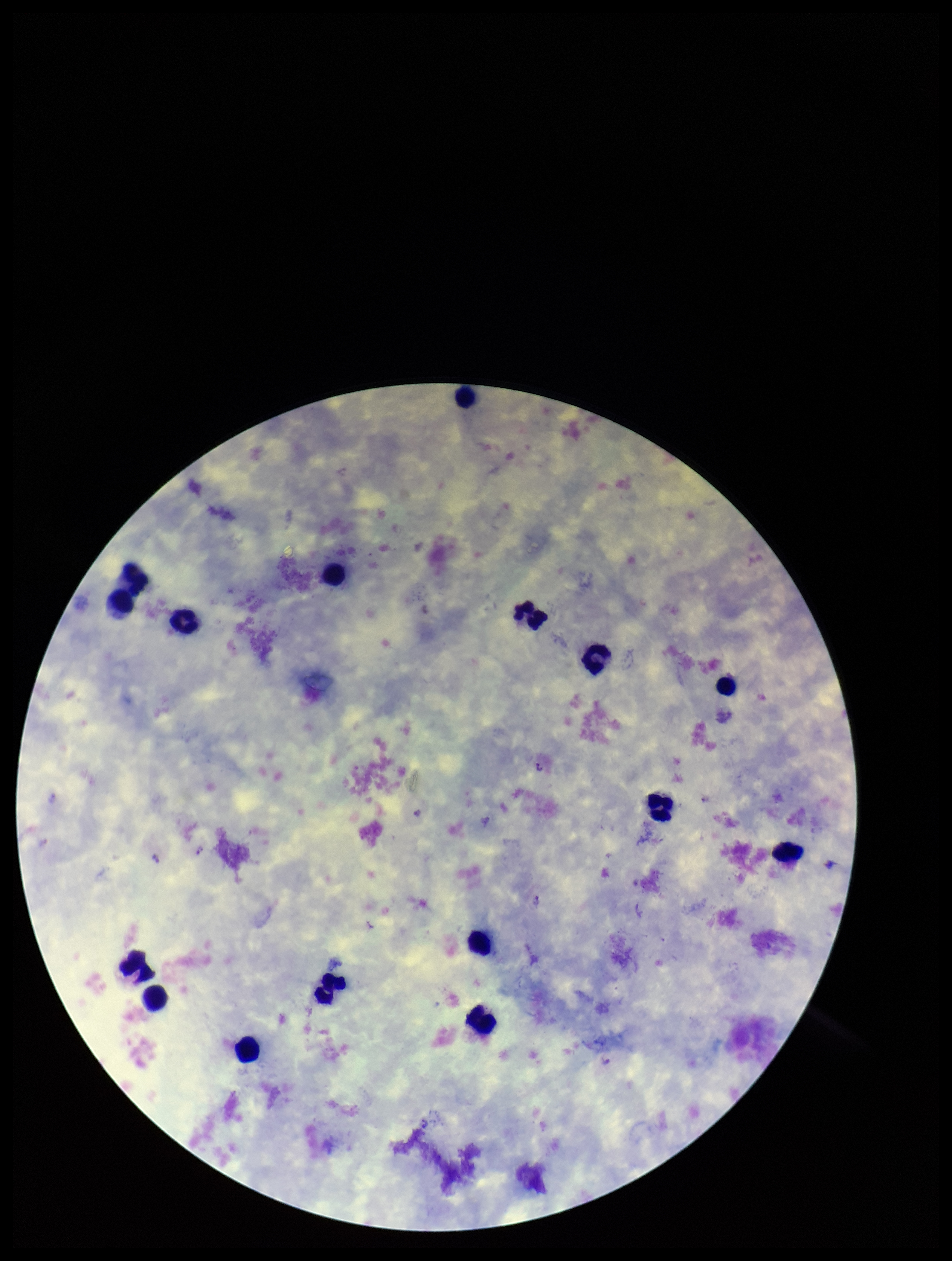

Smartphone photograph taken through the eyepiece of a microscope. Image is 952×1261 pixels. Patient malaria status: infected. Preparation: thick blood smear. Plasmodium parasites: seen. Parasite count: 7. Single field of view. Giemsa stain. Leukocyte count: 15. Species reported for this patient: Plasmodium vivax.